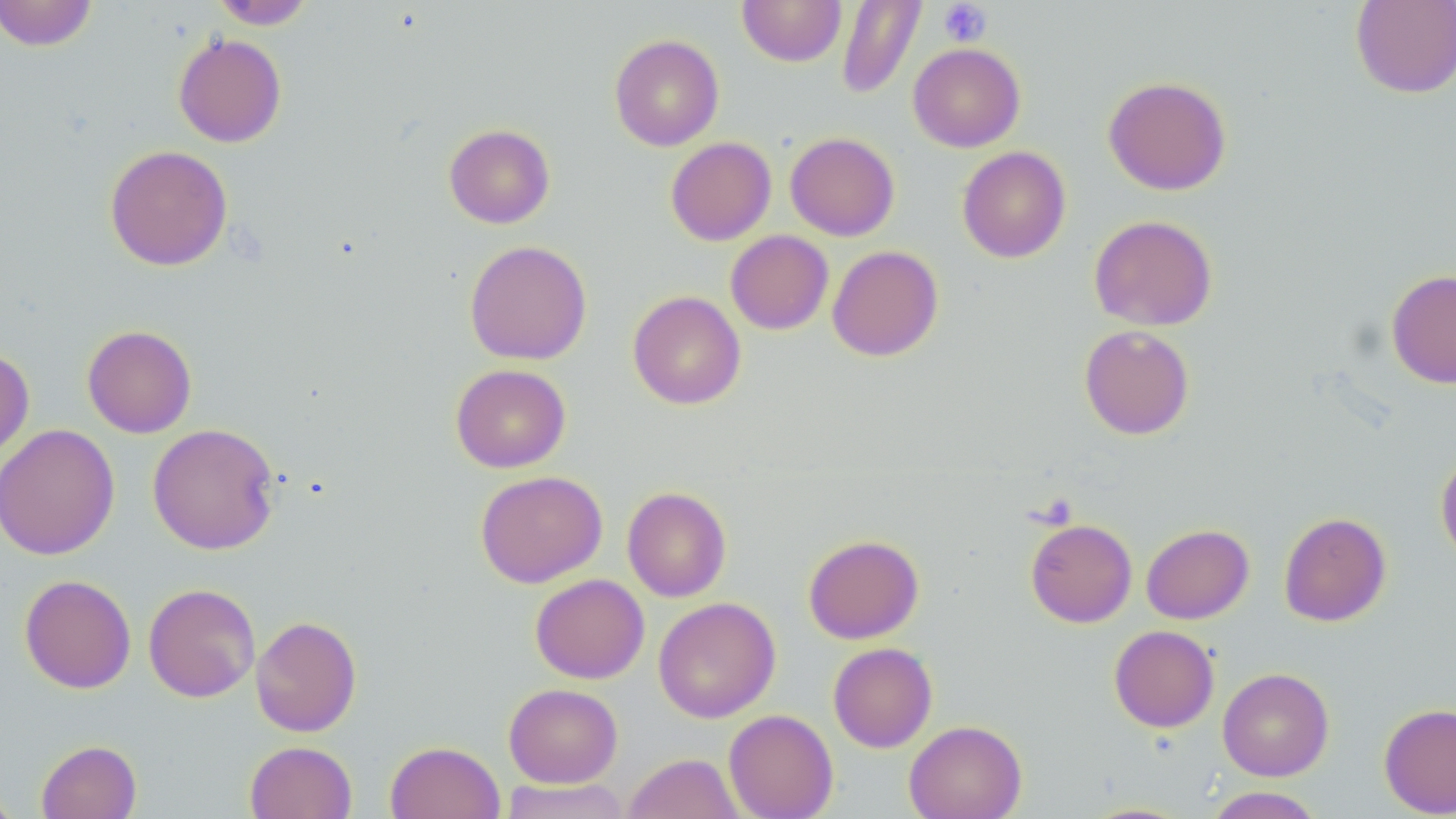

Summary:
  - Coordinate format: approximate bounding boxes as named x1/y1/x2/y2 corners in pixels
  - Platelet locations: (x1=938, y1=1, x2=991, y2=47)
  - Uninfected red blood cell locations: (x1=0, y1=0, x2=97, y2=52), (x1=737, y1=0, x2=846, y2=67), (x1=835, y1=0, x2=927, y2=100), (x1=1351, y1=0, x2=1456, y2=99), (x1=209, y1=1, x2=316, y2=29), (x1=173, y1=33, x2=287, y2=148), (x1=609, y1=34, x2=724, y2=151), (x1=908, y1=42, x2=1026, y2=152), (x1=1103, y1=75, x2=1232, y2=195), (x1=444, y1=123, x2=555, y2=228), (x1=785, y1=132, x2=900, y2=241), (x1=665, y1=137, x2=776, y2=245), (x1=104, y1=144, x2=233, y2=271), (x1=957, y1=146, x2=1071, y2=263), (x1=1089, y1=214, x2=1218, y2=332), (x1=725, y1=230, x2=834, y2=335), (x1=464, y1=239, x2=592, y2=365), (x1=827, y1=245, x2=943, y2=362), (x1=1386, y1=268, x2=1456, y2=389), (x1=627, y1=290, x2=746, y2=410), (x1=82, y1=324, x2=197, y2=438), (x1=1079, y1=324, x2=1195, y2=440), (x1=0, y1=347, x2=35, y2=462), (x1=450, y1=364, x2=571, y2=473), (x1=147, y1=423, x2=281, y2=555), (x1=0, y1=424, x2=120, y2=561), (x1=1435, y1=451, x2=1456, y2=565), (x1=475, y1=470, x2=608, y2=588), (x1=622, y1=486, x2=732, y2=602), (x1=1279, y1=512, x2=1391, y2=627), (x1=1025, y1=518, x2=1137, y2=628), (x1=1141, y1=523, x2=1254, y2=624), (x1=803, y1=534, x2=924, y2=644), (x1=19, y1=574, x2=136, y2=694), (x1=530, y1=574, x2=649, y2=683), (x1=143, y1=583, x2=261, y2=702), (x1=653, y1=597, x2=780, y2=723), (x1=250, y1=615, x2=362, y2=736), (x1=1109, y1=625, x2=1219, y2=732), (x1=827, y1=642, x2=938, y2=752), (x1=1217, y1=667, x2=1334, y2=781), (x1=503, y1=683, x2=622, y2=788), (x1=1378, y1=702, x2=1456, y2=817), (x1=723, y1=709, x2=838, y2=819), (x1=904, y1=720, x2=1027, y2=819), (x1=36, y1=740, x2=141, y2=819), (x1=384, y1=740, x2=504, y2=819), (x1=245, y1=741, x2=357, y2=819), (x1=623, y1=752, x2=745, y2=818), (x1=499, y1=778, x2=633, y2=819), (x1=0, y1=784, x2=21, y2=818), (x1=1202, y1=786, x2=1327, y2=819), (x1=1076, y1=801, x2=1197, y2=818)
  - Slide-level diagnosis: no evidence of blood parasites
  - Field of view: one of a larger specimen
  - Stain: May-Grünwald-Giemsa
  - Preparation: thin blood film
  - Magnification: 1000x
  - Image size: 1456×819 pixels
  - Modality: light microscopy